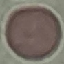
Result: no malaria parasites seen. Thin blood smear. Giemsa stain. Photographed with a smartphone camera at the microscope eyepiece. Automatically extracted cell patch, resized to 64 × 64 pixels.